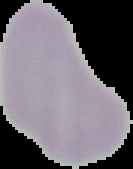
image type = cell region segmented out of the field of view; surrounding area masked to black
malaria status = uninfected
image size = 133×169 pixels
preparation = thin blood smear